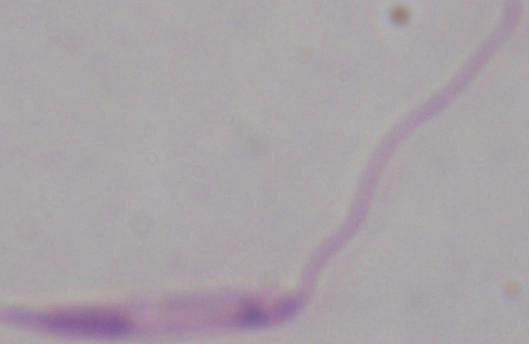 Photomicrograph. A Leishmania parasite is shown. Captured at 1000x magnification.